Give the position of every leukocyte.
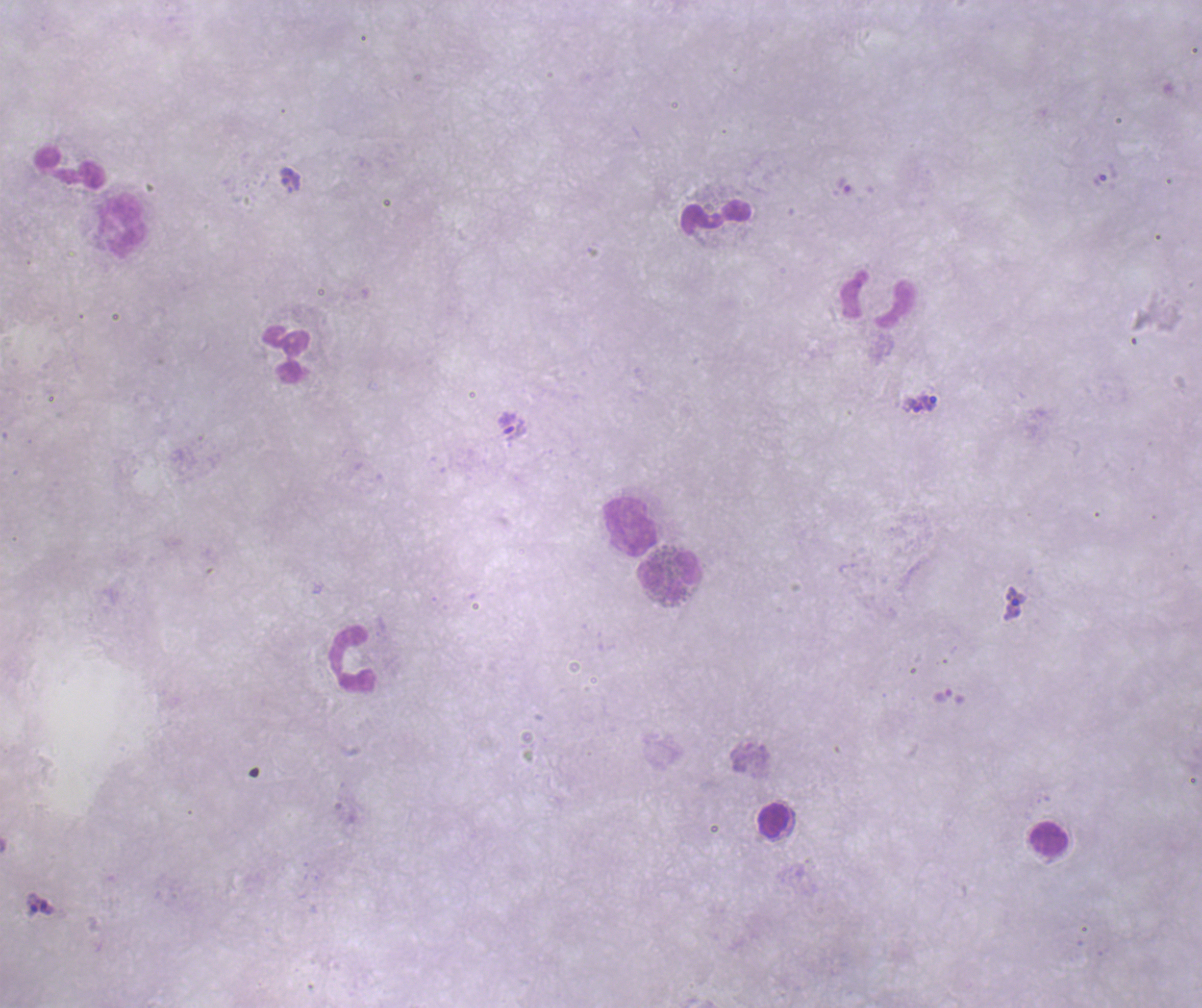

Approximate centers as (x, y) in pixels.
Leukocytes: (70, 166), (716, 217), (121, 226), (877, 298), (285, 354), (629, 527), (669, 577), (353, 659), (774, 821), (1048, 839).

Approximate centers as (x, y) in pixels.
Summary:
  - Trophozoite locations: (290, 180), (844, 185), (930, 403), (913, 405), (1014, 602), (33, 903), (48, 907)
  - Image size: 1202×1008 pixels
  - Magnification: 100x
  - Field of view: single
  - Preparation: thick blood smear
  - Context: previously used in a real diagnosis
  - Stain: Romanowsky
  - Result: Plasmodium parasites detected
  - Coloration quality: bad
  - Background quality: unsatisfactory